Give the position of every leukocyte visible.
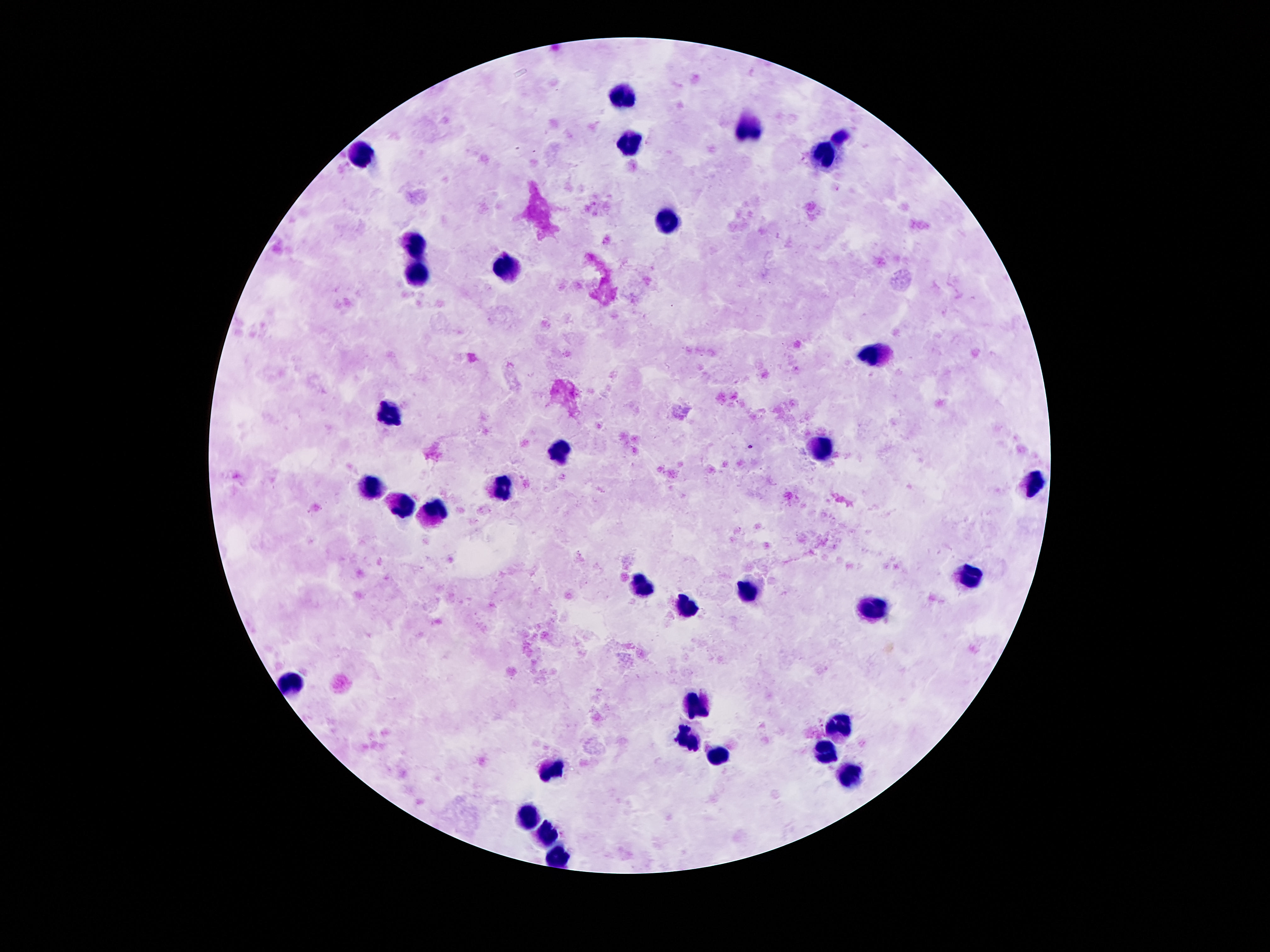

Approximate centers as {x, y} in pixels.
Leukocytes: {620, 94}, {745, 128}, {630, 145}, {362, 153}, {825, 159}, {665, 222}, {413, 249}, {505, 270}, {415, 272}, {878, 354}, {391, 411}, {825, 444}, {557, 448}, {1034, 483}, {370, 489}, {499, 489}, {401, 501}, {438, 511}, {970, 577}, {636, 587}, {743, 591}, {874, 605}, {684, 610}, {292, 683}, {698, 706}, {839, 724}, {688, 738}, {827, 753}, {718, 755}, {554, 769}, {847, 775}, {528, 814}, {548, 837}, {559, 857}.

One field from this slide. Patient malaria status: negative. Image is 1270×952 pixels. 100x magnification. Giemsa stain. Thick blood smear. Photographed through the microscope eyepiece with a smartphone camera.